Name the parasite shown.
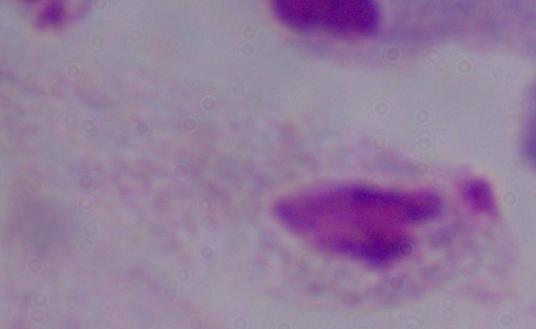
A trichomonad.

1000x magnification. Micrograph.